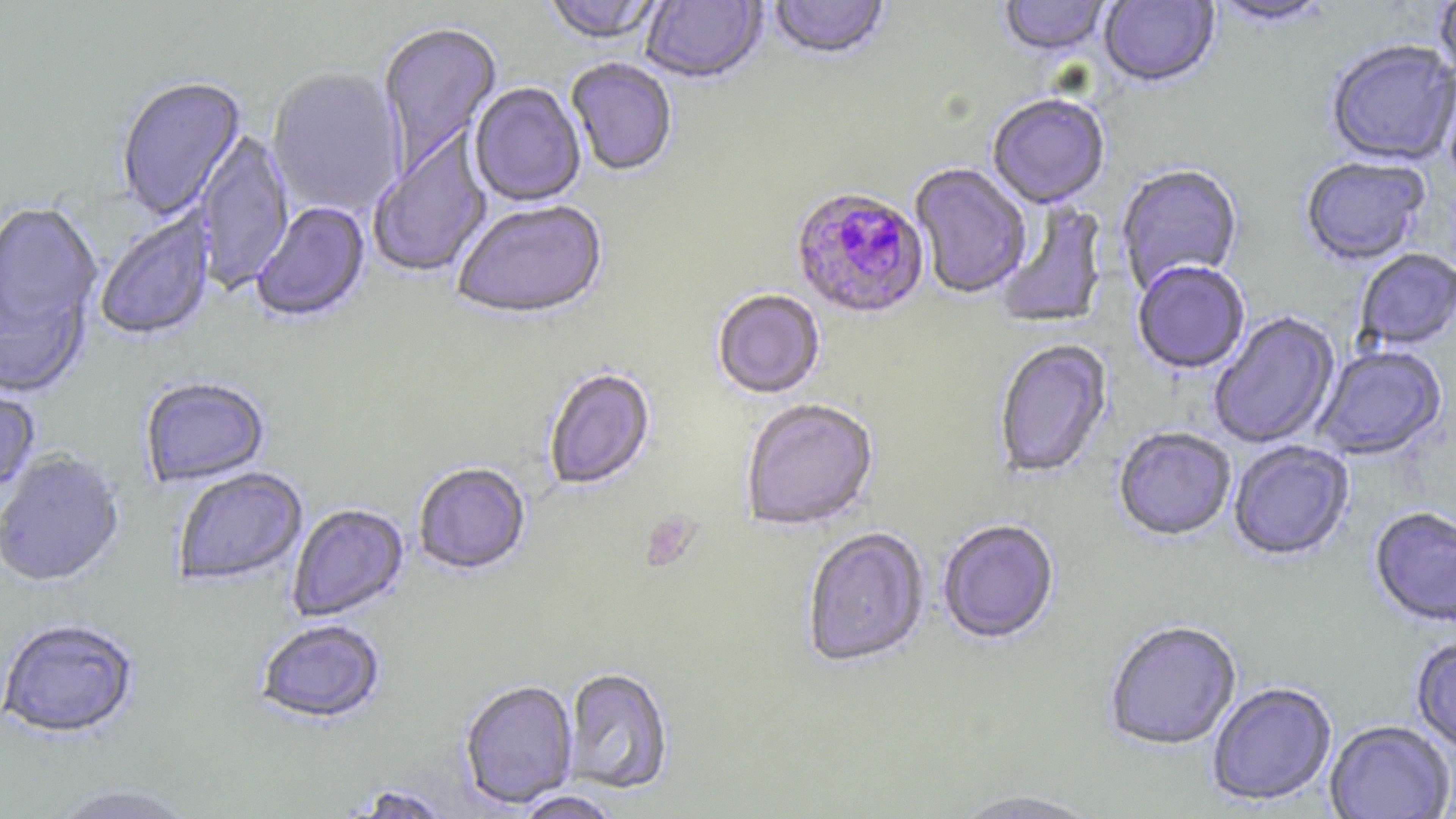

Approximate bounding boxes as (x1, y1, x2, y2) in pixels. Plasmodium falciparum-infected red blood cell locations: (790, 188, 929, 321). Uninfected red blood cell locations: (542, 0, 667, 47), (640, 0, 767, 87), (769, 0, 890, 63), (998, 0, 1113, 59), (1099, 0, 1220, 90), (1433, 0, 1456, 88), (1210, 1, 1336, 30), (377, 22, 502, 179), (1326, 41, 1456, 168), (566, 59, 678, 178), (1438, 64, 1456, 194), (266, 69, 404, 218), (117, 78, 247, 222), (469, 84, 586, 208), (987, 96, 1110, 211), (194, 129, 294, 294), (369, 131, 493, 281), (1300, 159, 1430, 268), (909, 164, 1031, 300), (1115, 166, 1243, 296), (996, 200, 1109, 329), (0, 201, 103, 359), (252, 202, 371, 325), (452, 202, 609, 324), (95, 210, 216, 343), (1355, 250, 1456, 352), (1132, 262, 1250, 376), (712, 291, 825, 401), (1209, 312, 1341, 450), (994, 341, 1113, 481), (1313, 346, 1448, 462), (543, 369, 656, 492), (140, 379, 270, 488), (0, 388, 41, 500), (740, 400, 879, 532), (1113, 428, 1236, 543), (1229, 442, 1354, 562), (0, 453, 125, 589), (413, 464, 531, 577), (172, 469, 308, 588), (287, 504, 409, 623), (1369, 508, 1456, 630), (938, 521, 1059, 646), (802, 528, 930, 670), (0, 620, 139, 741), (256, 621, 385, 725), (1104, 622, 1241, 752), (1410, 637, 1456, 755), (562, 669, 674, 795), (460, 681, 578, 809), (1207, 683, 1338, 807), (1325, 722, 1455, 819), (47, 785, 197, 819), (947, 790, 1104, 819), (512, 791, 624, 819). Platelet locations: (640, 512, 700, 573). Slide-level diagnosis: Plasmodium falciparum. Optical microscopy. Image is 1456×819 pixels. One field of a larger specimen. 1000x magnification. Thin blood smear. May-Grünwald-Giemsa stain.